Identify the parasite.
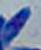

Toxoplasma gondii.

magnification = 1000x
modality = photomicrograph